Assess this cell for malaria.
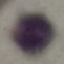
Uninfected.

preparation = thin blood film
stain = Giemsa
capture = smartphone camera at the microscope eyepiece
image type = automatically extracted cell patch, resized to 64 × 64 pixels